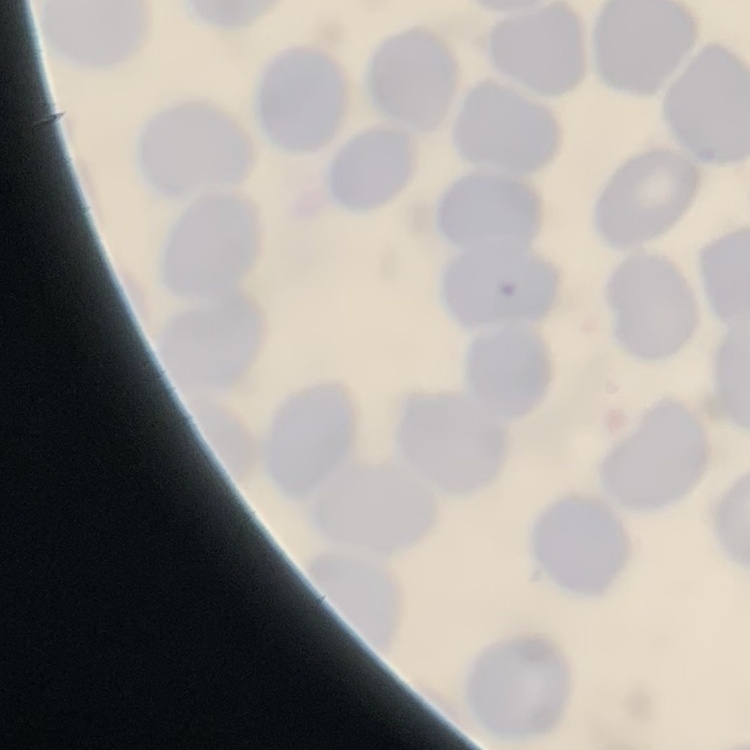
{
  "erythrocyte_morphology": "no rouleaux formation",
  "stain": "Field's or Giemsa",
  "image_type": "one tile cut from a larger photomicrograph",
  "preparation": "thin blood film"
}